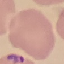
Summary:
  - Result: malaria parasites detected
  - Stain: Giemsa
  - Capture: smartphone camera at the microscope eyepiece
  - Preparation: thin blood smear
  - Image type: cell patch, automatically extracted from a larger field of view and resized to 64 × 64 pixels